Classify this cell by malaria status.
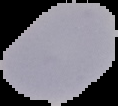

Uninfected.

Image is 118×106 pixels. From a thin blood film. Cell region segmented out of the field of view; the surrounding area is masked to black.